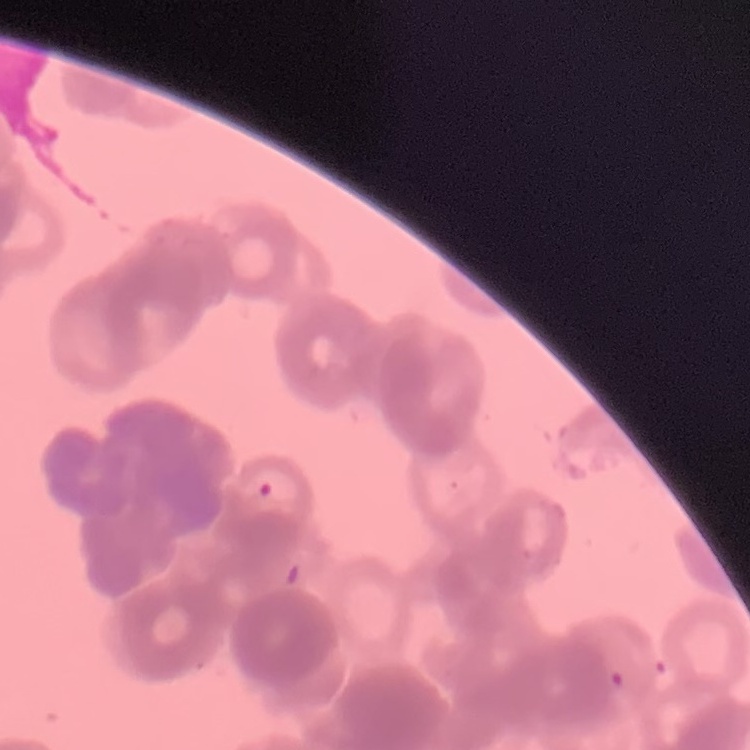

The erythrocytes show rouleaux formation. Thin blood film. Stained with either Field's or Giemsa. One tile cut from a larger photomicrograph.